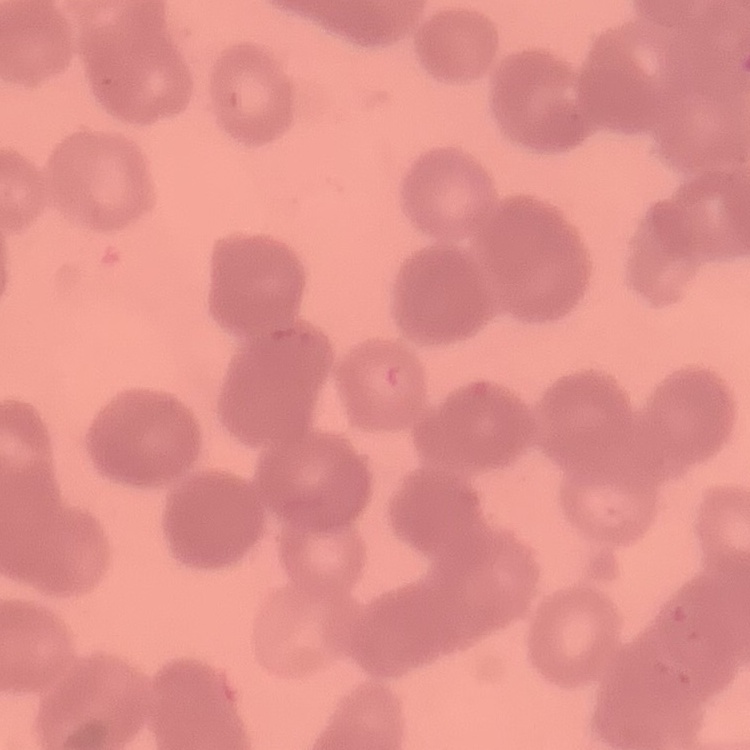
{
  "red_blood_cell_morphology": "rouleaux formation",
  "image_type": "square crop of a larger photomicrograph",
  "stain": "Field's or Giemsa",
  "preparation": "thin peripheral smear"
}